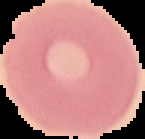
Image is 145×139 pixels. From a thin blood smear. The area outside the segmented cell region is set to black. Malaria status: uninfected.